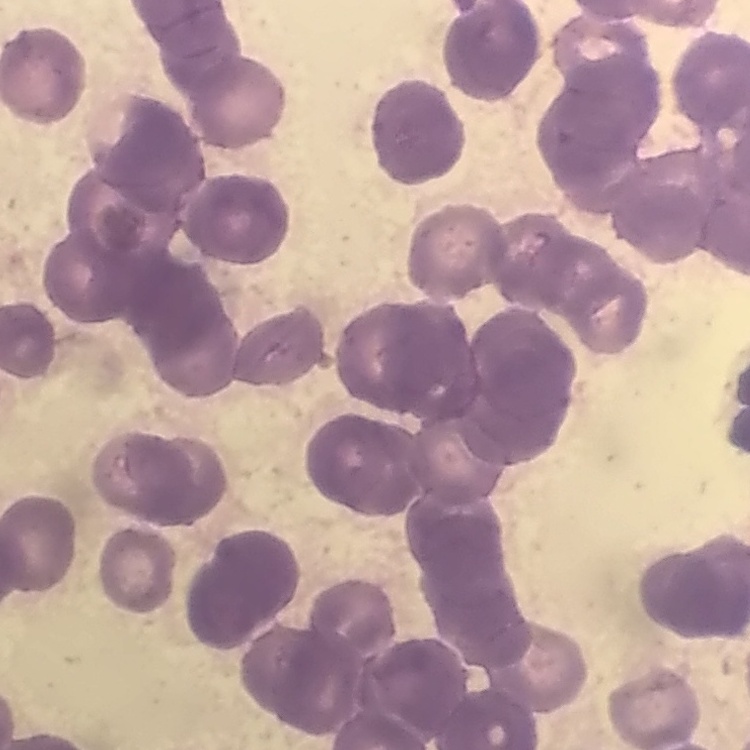

erythrocyte_morphology: rouleaux formation
preparation: thin peripheral smear
image_type: one tile cut from a larger photomicrograph
stain: Field's or Giemsa